Give the position of every malaria parasite.
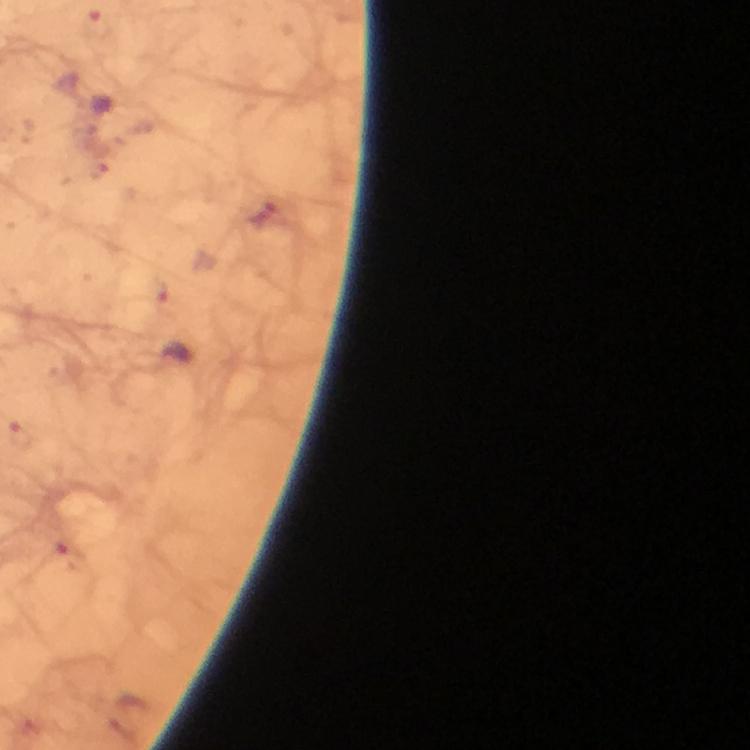

Approximate centers as (x, y) in pixels.
Malaria parasites: (261, 212).

From a malaria diagnostic workup. Immersion oil was used. A crop from one field of view. Giemsa stain. Photographed with a smartphone mounted on the microscope. Thick blood smear. Image is 750×750 pixels. At 100x magnification.